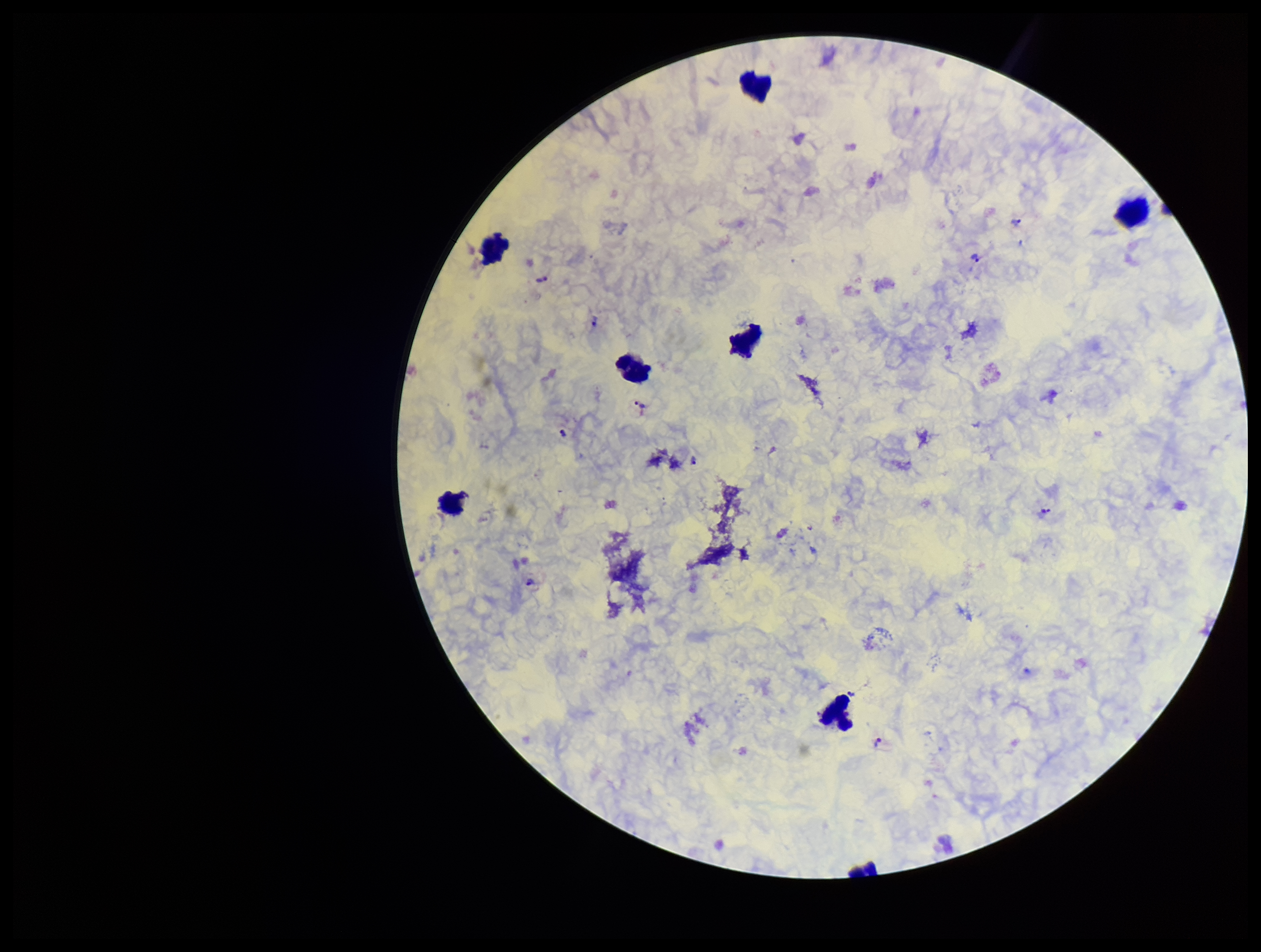

parasite count = 10
preparation = thick blood smear
patient malaria status = infected
leukocyte count = 7
image size = 1261×952 pixels
field of view = single
species reported for this patient = Plasmodium vivax
capture = smartphone photograph through the microscope eyepiece
stain = Giemsa
Plasmodium parasites = seen